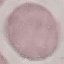
Summary:
  - Malaria status: uninfected
  - Capture: smartphone through the microscope eyepiece
  - Image type: automatically extracted cell patch, resized to 64 × 64 pixels
  - Stain: Giemsa
  - Preparation: thin blood smear